Assess this cell for malaria.
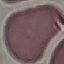

Uninfected.

Giemsa stain. Thin smear of blood. Automatically extracted cell patch, resized to 64 × 64 pixels. Acquired by smartphone through the microscope eyepiece.